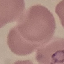

Malaria status: parasitized. Automatically extracted cell patch, resized to 64 × 64 pixels. Thin blood smear. Photographed with a smartphone camera at the microscope eyepiece. Giemsa-stained preparation.